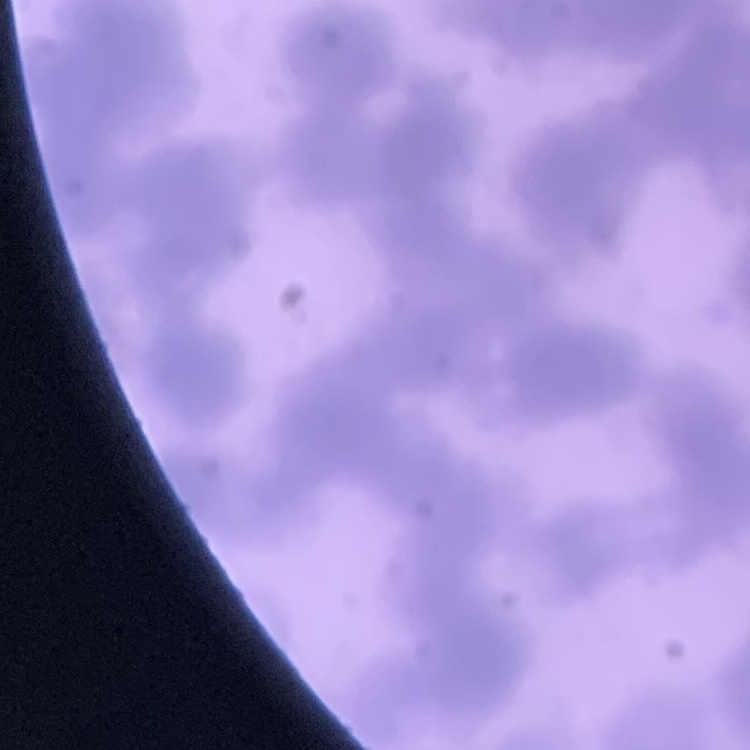

erythrocyte morphology = rouleaux formation
image type = square crop of a larger photomicrograph
preparation = thin blood film
stain = Field's or Giemsa